Point out each Plasmodium parasite.
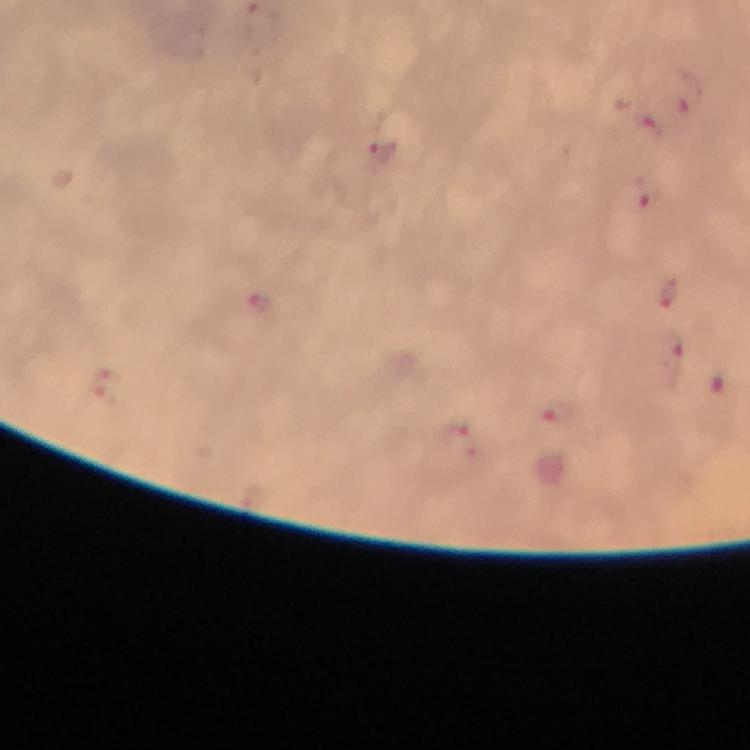

Approximate centers as (x, y) in pixels.
Plasmodium parasites: (689, 95), (646, 123), (383, 153), (666, 295), (258, 305), (670, 356), (103, 385), (557, 411), (464, 440).

Summary:
  - Preparation: thick smear
  - Stain: Giemsa
  - Capture: smartphone photograph through a microscope
  - Magnification: 100x
  - Immersion oil: used
  - Cropped from: one field of view
  - Context: from a malaria diagnostic workup
  - Image size: 750×750 pixels